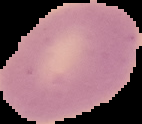
Summary:
  - Image size: 142×124 pixels
  - Result: negative for malaria parasites
  - Image type: segmented cell region on a black background
  - Preparation: thin blood film